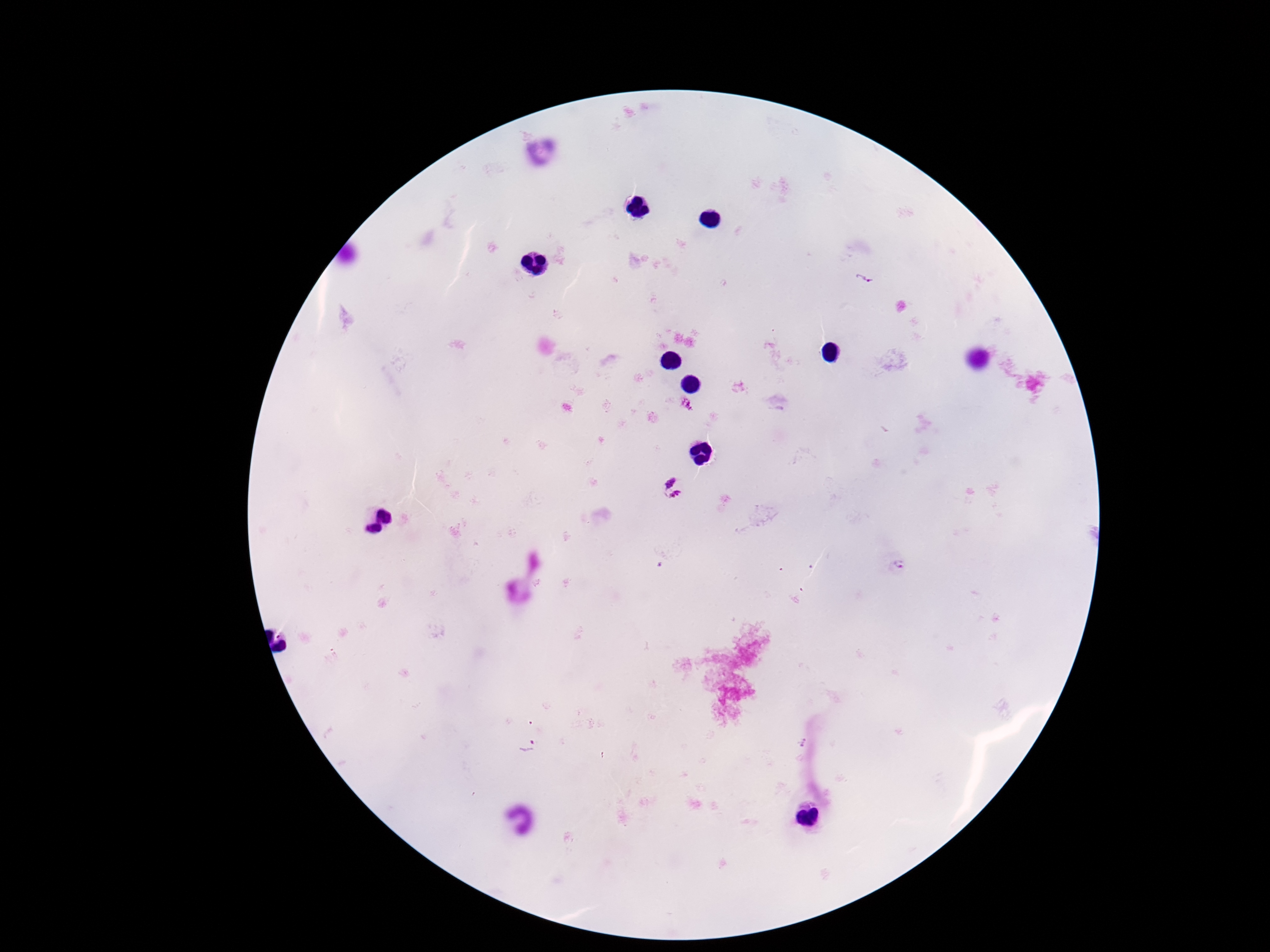
Approximate centers as (x, y) in pixels. Plasmodium parasite locations: (864, 278), (665, 479), (677, 499), (899, 567), (527, 746). One field from this slide. Patient malaria status: positive. Thick blood film. 100x magnification. Giemsa stain. Image is 1270×952 pixels. Smartphone photograph taken through the microscope eyepiece.